Locate and identify every blood parasite.
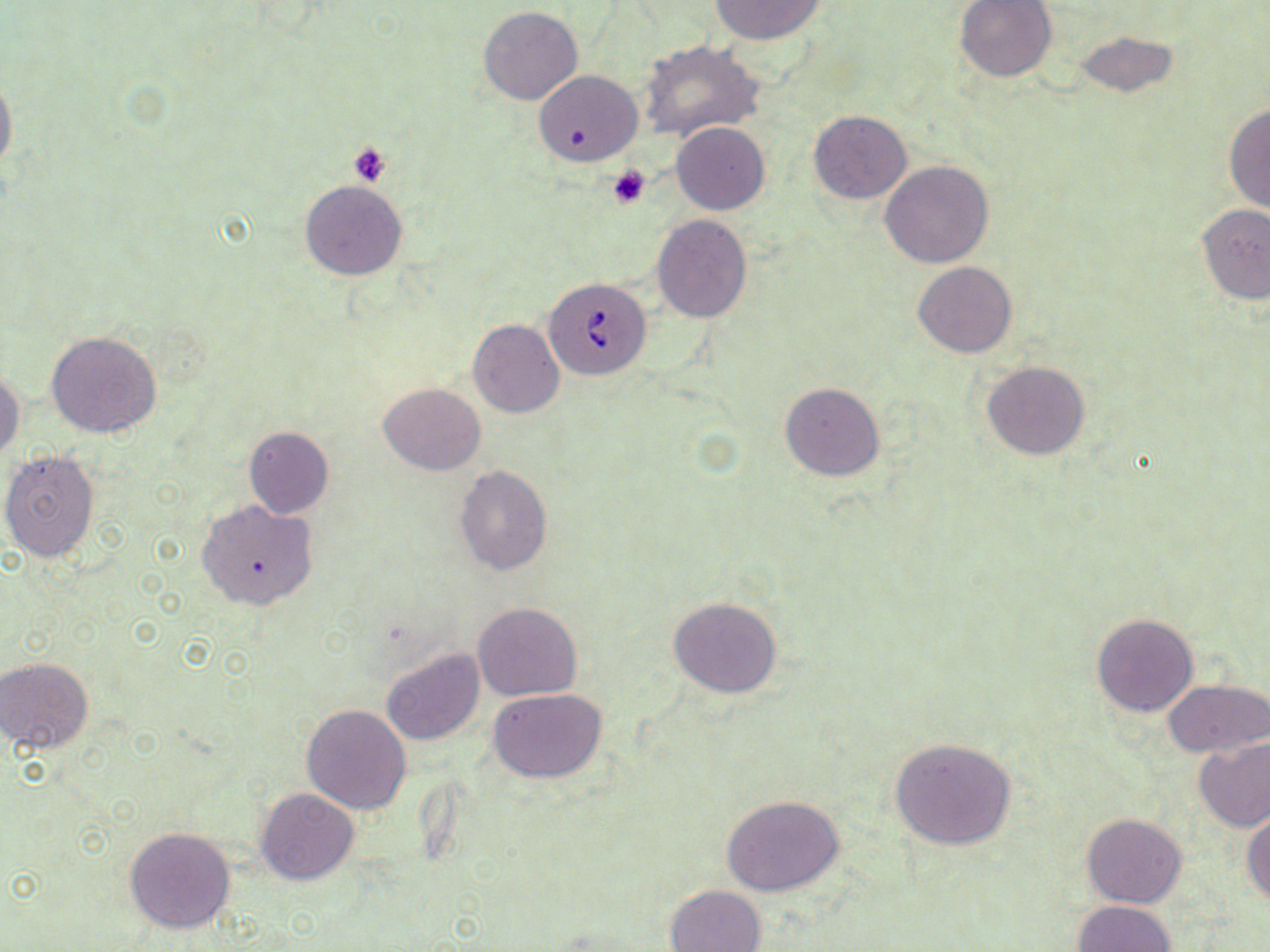
Approximate bounding boxes as [x1, y1, x2, y2] in pixels.
Babesia divergens-infected red blood cells: [543, 276, 651, 379].
No Plasmodium falciparum, Plasmodium ovale, Plasmodium malariae, Plasmodium vivax, or Trypanosoma brucei observed.

Uninfected red blood cell locations: [708, 0, 828, 46], [954, 0, 1057, 82], [478, 6, 582, 105], [1074, 30, 1181, 99], [638, 40, 765, 143], [535, 70, 643, 166], [0, 72, 17, 176], [1223, 103, 1270, 215], [809, 111, 911, 203], [672, 122, 769, 214], [880, 160, 994, 268], [300, 180, 407, 281], [1196, 204, 1270, 305], [652, 215, 751, 321], [913, 261, 1017, 358], [467, 320, 564, 418], [46, 331, 163, 439], [980, 361, 1089, 460], [0, 368, 24, 464], [780, 382, 884, 480], [377, 383, 485, 475], [244, 427, 333, 518], [1, 452, 100, 561], [454, 465, 552, 575], [196, 499, 318, 610], [668, 597, 782, 697], [472, 601, 582, 701], [1091, 613, 1198, 718], [381, 648, 484, 745], [1, 657, 94, 754], [1164, 677, 1270, 759], [489, 687, 608, 783], [302, 704, 412, 812], [889, 738, 1017, 849], [1193, 738, 1270, 831], [255, 788, 358, 884], [721, 795, 845, 896], [1243, 811, 1270, 908], [1082, 813, 1187, 908], [124, 828, 235, 933], [665, 883, 767, 952], [1073, 900, 1175, 952]. Platelet locations: [348, 142, 391, 187], [607, 165, 651, 208]. Slide-level diagnosis: Babesia divergens. May-Grünwald-Giemsa stain. Single field of view. 1000x magnification. Image is 1270×952 pixels. Light microscopy. Thin blood film.